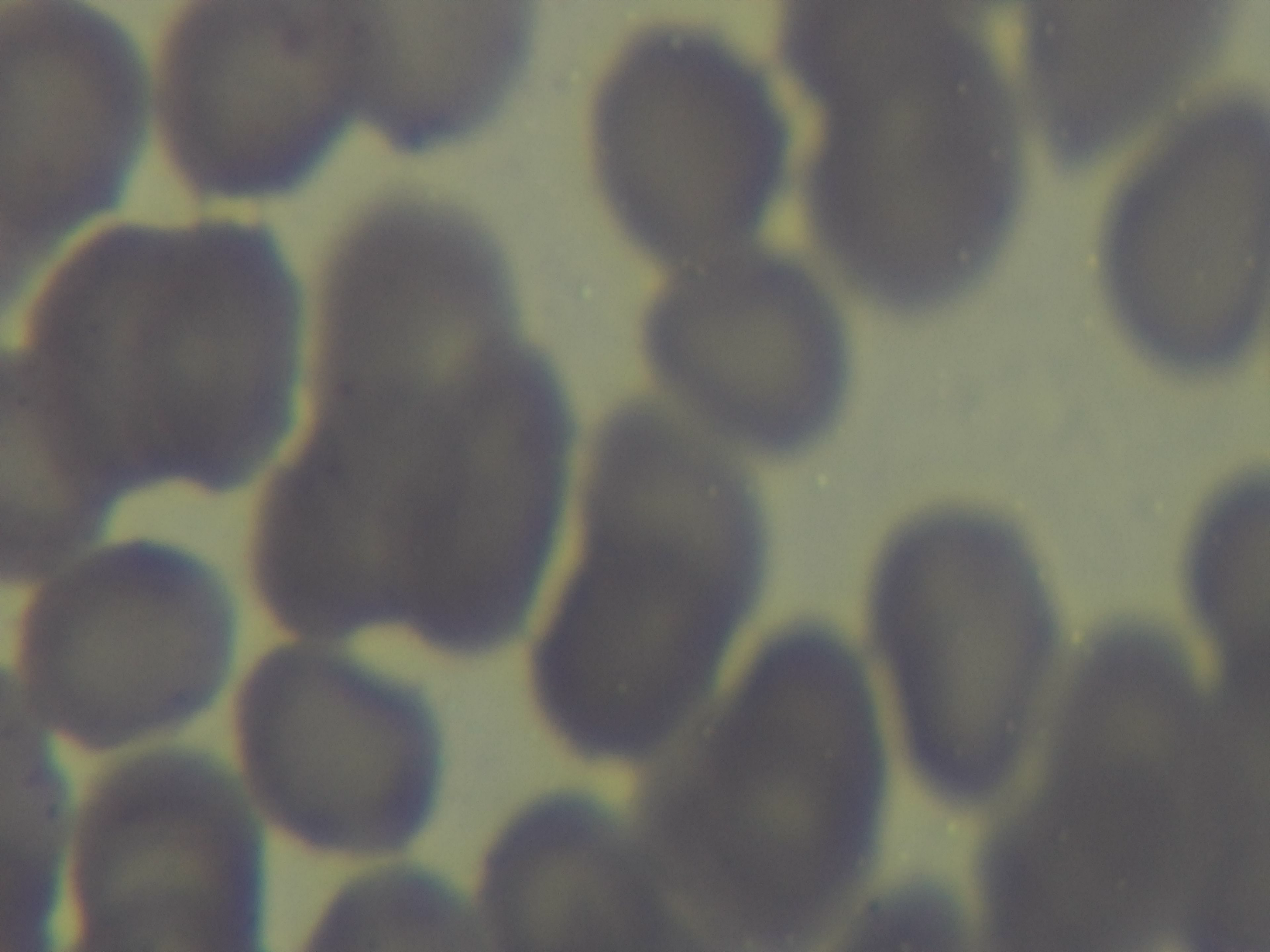

Summary:
  - Capture: mounted 4K digital camera
  - Stain: Giemsa
  - Modality: light microscopy
  - Objective: 100x oil immersion
  - Malaria status: negative
  - Preparation: thin smear
  - Field of view: one from the slide